Report the malaria status of this cell.
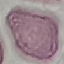
It is uninfected.

Thin blood smear. Giemsa-stained preparation. Automatically extracted cell patch, resized to 64 × 64 pixels. Photographed with a smartphone camera at the microscope eyepiece.